Give the preparation type.
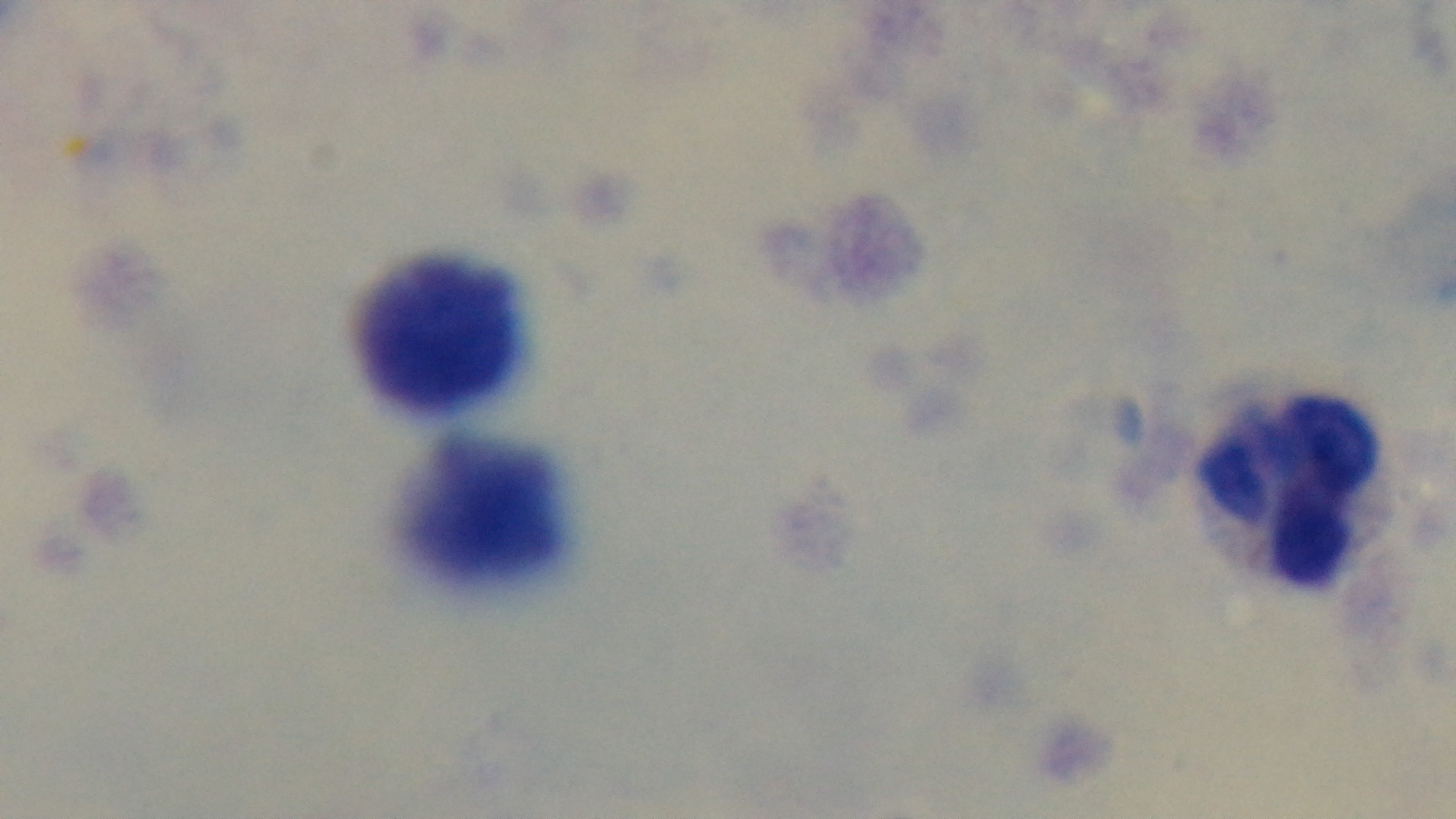

Thick.

stain: Giemsa
field_of_view: one from the slide
objective: 100x oil immersion
malaria_status: negative
modality: light microscopy
capture: mounted 4K digital camera